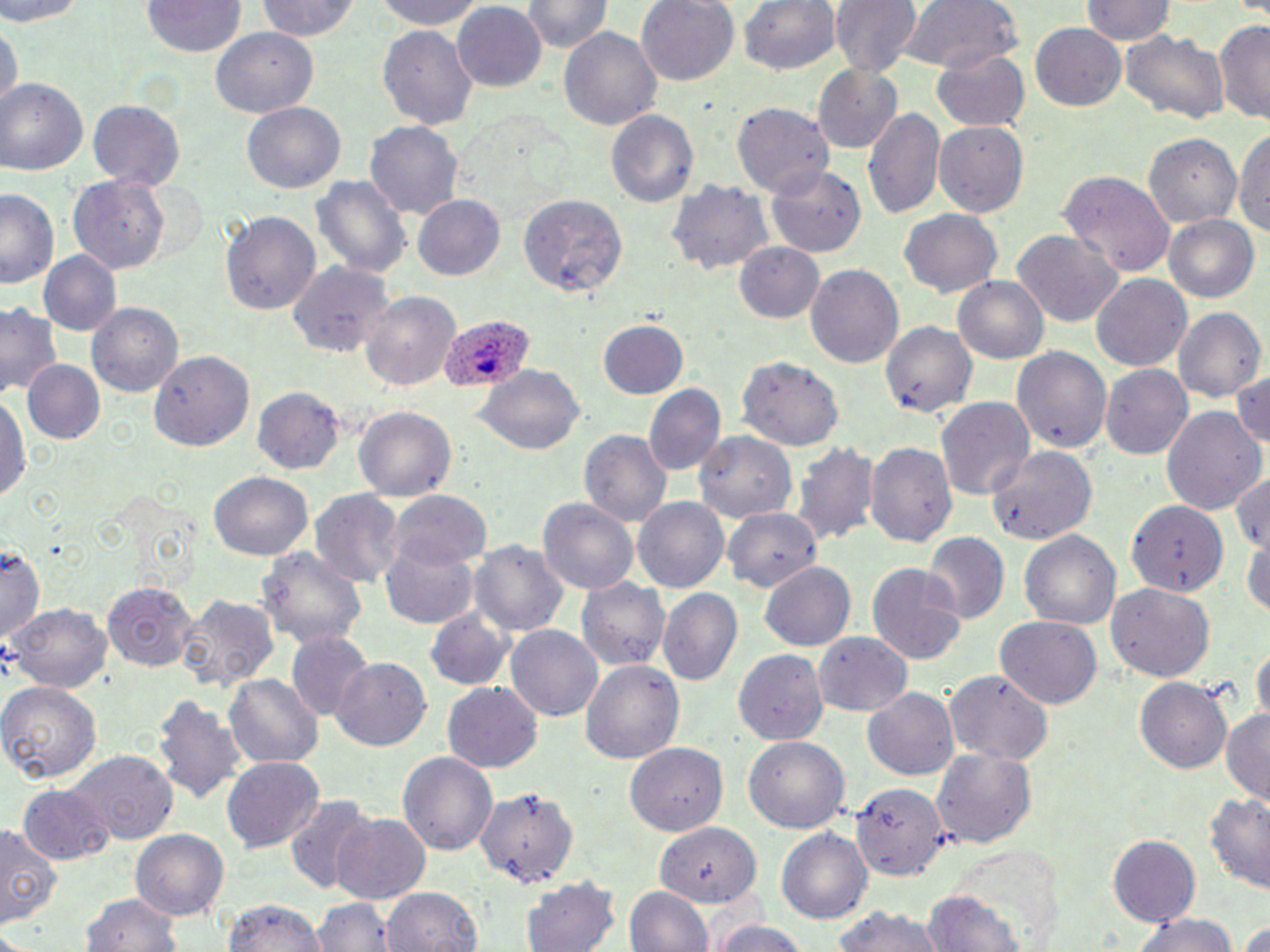

slide_level_diagnosis: Plasmodium ovale
image_size: 1270×952 pixels
modality: optical microscopy
preparation: thin blood smear
uninfected_red_blood_cell_locations: 'approximate bounding boxes as [x1, y1, x2, y2] in pixels: [0, 0, 88, 24], [258, 0, 367, 44], [375, 0, 492, 32], [637, 0, 739, 87], [738, 0, 841, 76], [831, 0, 920, 77], [896, 0, 1025, 75], [1082, 0, 1175, 46], [522, 1, 611, 56], [142, 2, 246, 59], [452, 2, 547, 90], [1215, 19, 1270, 123], [0, 20, 19, 116], [1029, 20, 1128, 111], [558, 24, 663, 129], [211, 27, 317, 117], [376, 28, 477, 126], [1119, 31, 1231, 125], [930, 46, 1031, 131], [815, 65, 904, 153], [2, 79, 88, 175], [87, 99, 185, 187], [242, 102, 344, 193], [732, 104, 835, 197], [864, 107, 944, 222], [607, 108, 699, 208], [367, 121, 463, 220], [933, 122, 1030, 217], [1235, 125, 1270, 246], [1143, 132, 1245, 229], [767, 164, 868, 257], [1059, 169, 1177, 274], [311, 173, 411, 283], [69, 175, 172, 274], [669, 178, 774, 276], [1, 189, 61, 292], [520, 194, 628, 298], [413, 197, 505, 279], [898, 208, 1004, 297], [223, 211, 321, 315], [1164, 215, 1260, 303], [1012, 229, 1124, 326], [736, 241, 826, 325], [40, 251, 120, 337], [287, 262, 394, 357], [804, 263, 904, 370], [1090, 272, 1193, 373], [955, 275, 1048, 363], [357, 290, 463, 393], [0, 300, 61, 403], [88, 302, 184, 397], [1174, 306, 1264, 406], [596, 320, 689, 400], [881, 320, 978, 420], [1010, 344, 1113, 453], [151, 350, 251, 452], [735, 357, 843, 451], [23, 359, 105, 445], [1100, 364, 1194, 460], [1231, 366, 1269, 452], [477, 367, 584, 455], [644, 384, 725, 476], [253, 388, 342, 472], [2, 395, 30, 508], [935, 395, 1036, 500], [1160, 404, 1267, 514], [354, 406, 455, 505], [578, 428, 672, 530], [696, 431, 797, 523], [866, 441, 957, 548], [793, 442, 878, 546], [987, 444, 1097, 545], [1231, 468, 1269, 555], [210, 473, 312, 561], [311, 489, 403, 587], [388, 489, 493, 567], [539, 496, 640, 595], [634, 496, 732, 593], [1126, 500, 1230, 596], [722, 508, 820, 592], [1020, 530, 1121, 634], [923, 533, 1008, 624], [1244, 533, 1270, 620], [380, 536, 481, 629], [470, 538, 569, 638], [3, 543, 46, 643], [259, 547, 365, 652], [866, 561, 968, 666], [760, 563, 853, 650], [103, 579, 198, 670], [577, 579, 670, 672], [1107, 584, 1217, 683], [656, 588, 743, 686], [176, 593, 282, 690], [8, 604, 113, 694], [425, 607, 513, 692], [993, 616, 1101, 709], [507, 625, 604, 721], [288, 632, 371, 722], [815, 633, 911, 717], [1252, 640, 1269, 729], [736, 649, 827, 743], [332, 656, 435, 751], [579, 659, 685, 767], [946, 670, 1054, 763], [227, 673, 323, 768], [1135, 676, 1232, 775], [0, 680, 103, 785], [442, 683, 543, 772], [864, 689, 959, 779], [152, 696, 247, 803], [1220, 707, 1270, 802], [742, 736, 850, 834], [626, 742, 725, 835], [930, 746, 1037, 848], [398, 749, 497, 858], [69, 752, 176, 844], [223, 757, 323, 853], [17, 783, 114, 867], [473, 785, 577, 887], [852, 785, 947, 880], [1204, 790, 1270, 892], [284, 795, 377, 895], [333, 812, 431, 903], [0, 825, 58, 926], [655, 826, 759, 908], [777, 829, 872, 922], [132, 830, 228, 919], [1107, 832, 1202, 924], [946, 844, 1070, 950], [522, 875, 622, 952], [625, 885, 715, 952], [382, 886, 483, 952], [82, 888, 188, 952], [925, 891, 1024, 952], [316, 895, 393, 951], [222, 897, 329, 952], [828, 906, 951, 952], [1127, 913, 1241, 952], [1235, 918, 1270, 952], [704, 919, 818, 952]'
stain: May-Grünwald-Giemsa
plasmodium_ovale_infected_red_blood_cell_locations: 'approximate bounding boxes as [x1, y1, x2, y2] in pixels: [438, 313, 535, 393]'
field_of_view: one of a larger specimen
magnification: 1000x